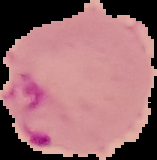

image size = 157×160 pixels
preparation = thin blood film
result = malaria parasites detected
image type = segmented cell region with the area outside set to black